Report the malaria status of this cell.
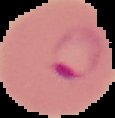

It is parasitized.

Segmented cell region on a black background. From a thin blood smear. Image is 115×118 pixels.